Assess this cell for malaria.
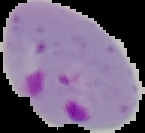
Parasitized.

Cell region segmented out of the field of view; the surrounding area is masked to black. From a thin blood smear. Image is 145×133 pixels.